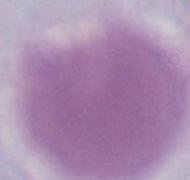
An erythrocyte is shown. Photomicrograph. 1000x magnification.